Assess this cell for malaria.
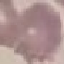
It is uninfected.

Giemsa stain. Thin blood film. Acquired by smartphone through the microscope eyepiece. Automatically extracted cell patch, resized to 64 × 64 pixels.